Report the malaria status of this cell.
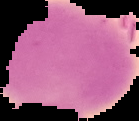

It is uninfected.

Image is 139×121 pixels. Segmented cell region on a black background. From a thin blood smear.